Assess this cell for malaria.
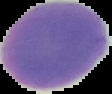

It is uninfected.

{
  "image_size": "112×94 pixels",
  "preparation": "thin blood film",
  "image_type": "segmented cell region with the area outside set to black"
}